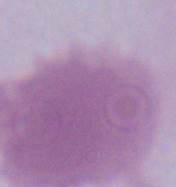 An erythrocyte is seen. Photomicrograph. Captured at 1000x magnification.